Locate every Plasmodium parasite.
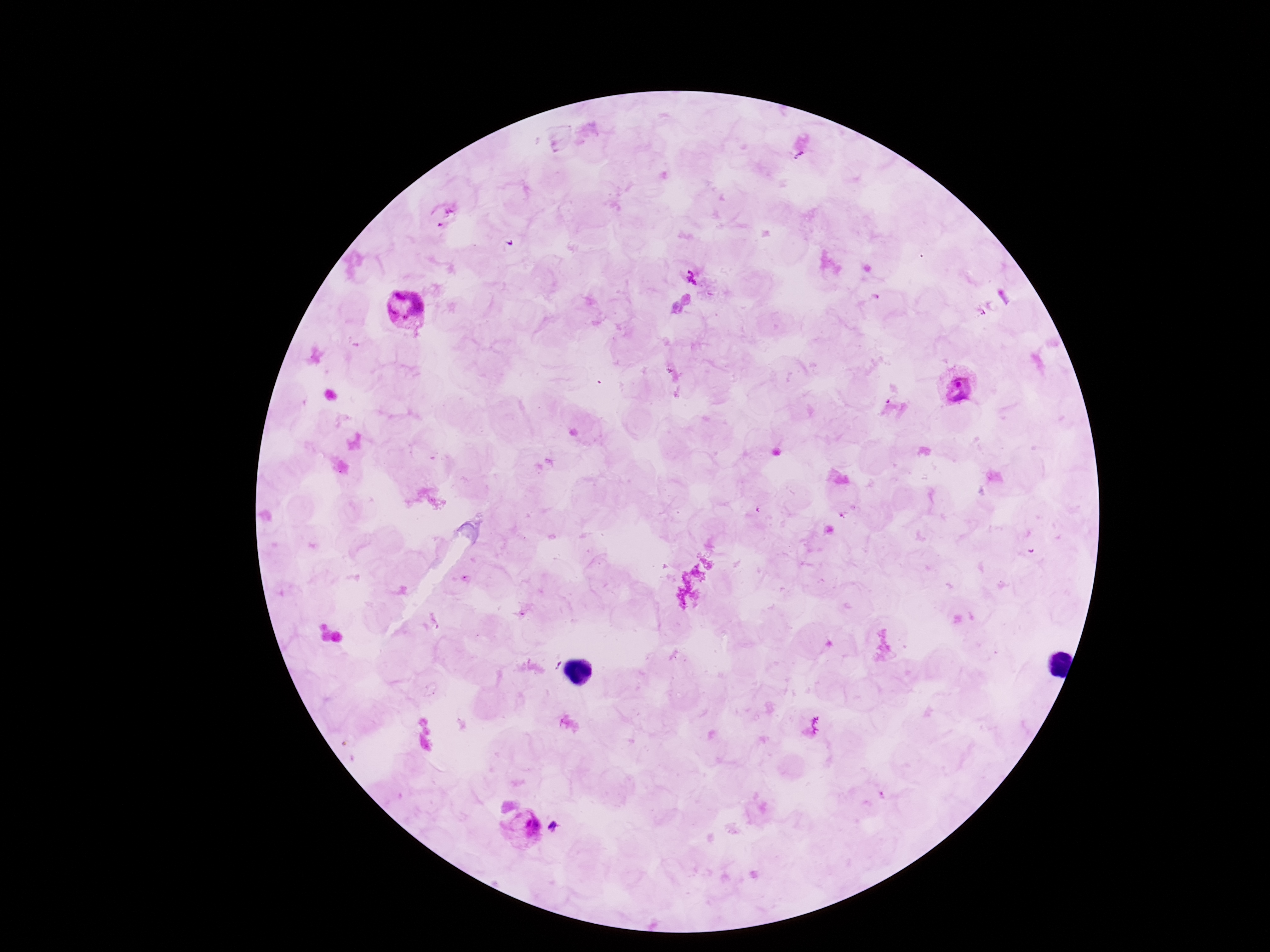
Approximate centers as (x, y) in pixels.
Plasmodium parasites: (691, 273), (404, 311), (958, 387), (523, 829).

Summary:
  - Magnification: 100x
  - Preparation: thick blood smear
  - Stain: Giemsa
  - Field of view: single
  - Capture: smartphone camera through the microscope eyepiece
  - Image size: 1270×952 pixels
  - Patient malaria status: positive